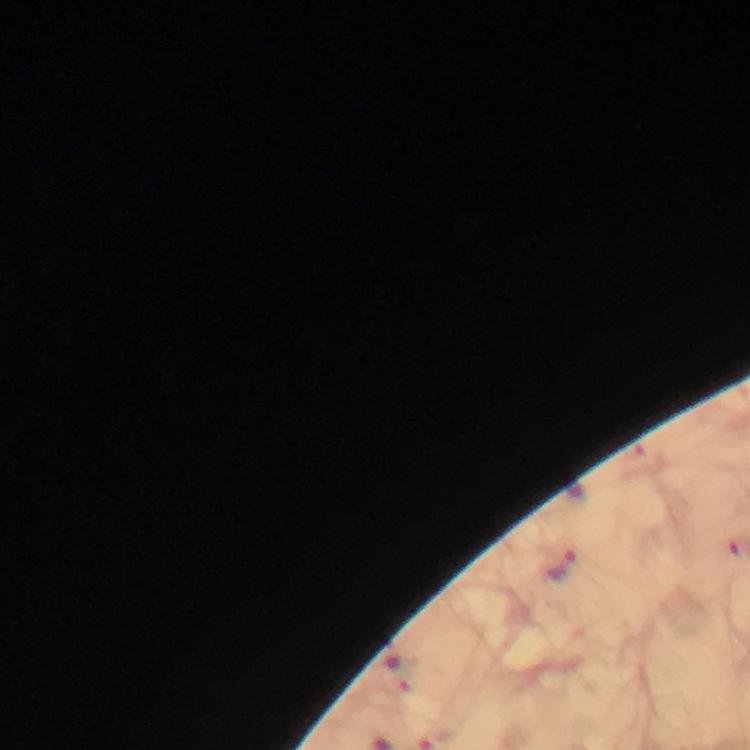
magnification = 100x
image size = 750×750 pixels
cropped from = one field of view
capture = smartphone camera through the microscope
Plasmodium parasite locations = approximate centers as {x, y} in pixels: {561, 565}, {396, 672}
context = from a diagnostic examination for malaria
stain = Giemsa
preparation = thick blood film
immersion oil = applied